Identify the blood parasite species.
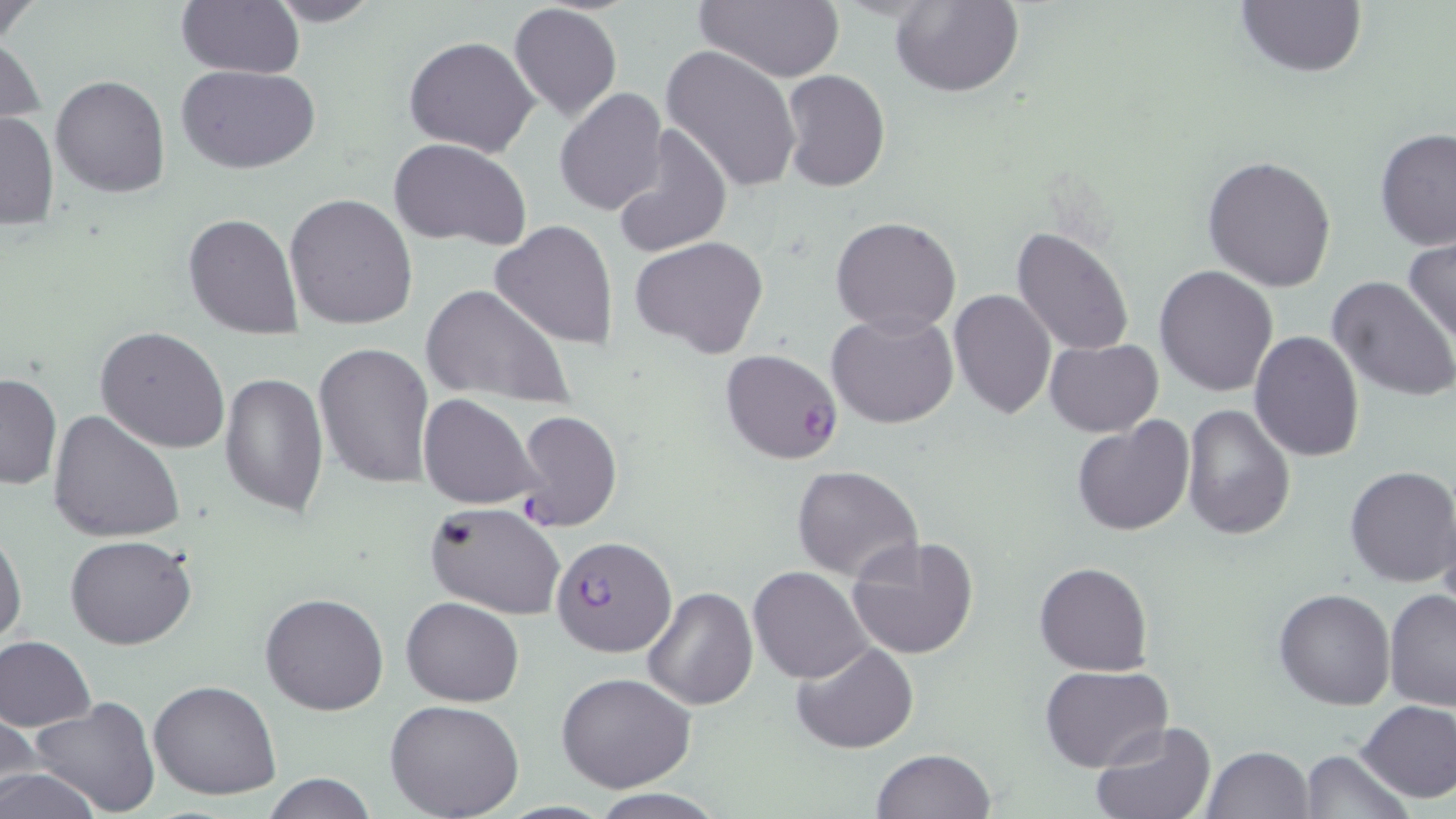
Plasmodium falciparum.

Summary:
  - Coordinate format: approximate bounding boxes as (x1, y1, x2, y2) in pixels
  - Plasmodium falciparum-infected red blood cell locations: (720, 350, 842, 464), (550, 535, 678, 657)
  - Uninfected red blood cell locations: (0, 0, 46, 49), (174, 0, 304, 78), (261, 0, 383, 26), (694, 0, 844, 81), (892, 0, 1023, 97), (1234, 1, 1367, 79), (507, 3, 623, 122), (1, 31, 47, 137), (404, 36, 540, 158), (659, 45, 801, 194), (176, 64, 322, 172), (781, 69, 890, 192), (50, 75, 170, 198), (555, 89, 670, 215), (0, 110, 59, 230), (611, 126, 733, 258), (1375, 129, 1456, 250), (387, 137, 531, 249), (1202, 154, 1337, 292), (284, 192, 419, 330), (183, 213, 303, 337), (831, 216, 962, 335), (489, 220, 620, 351), (1012, 226, 1136, 357), (1403, 234, 1456, 349), (631, 235, 770, 359), (1153, 264, 1278, 397), (1327, 275, 1456, 404), (421, 283, 572, 406), (948, 289, 1057, 419), (828, 310, 958, 429), (96, 326, 230, 454), (1248, 331, 1364, 463), (1044, 338, 1164, 435), (313, 341, 435, 488), (219, 372, 330, 517), (1, 373, 62, 491), (419, 393, 541, 510), (1181, 402, 1295, 540), (47, 408, 186, 543), (514, 408, 623, 532), (1072, 415, 1194, 537), (792, 464, 923, 584), (1343, 465, 1455, 587), (1436, 498, 1456, 618), (425, 502, 568, 620), (0, 522, 26, 647), (65, 534, 197, 650), (846, 534, 981, 660), (1034, 562, 1152, 676), (748, 565, 873, 683), (642, 587, 757, 710), (1273, 588, 1396, 710), (1383, 588, 1456, 710), (260, 592, 389, 716), (402, 597, 525, 706), (0, 635, 96, 731), (793, 641, 916, 754), (1040, 664, 1172, 771), (556, 673, 698, 791), (148, 680, 281, 802), (385, 698, 525, 819), (30, 699, 162, 818), (1357, 699, 1456, 802), (1, 705, 42, 806), (1090, 721, 1216, 819), (1201, 745, 1313, 819), (870, 748, 997, 819), (1298, 749, 1412, 819), (0, 765, 104, 819), (261, 774, 381, 818)
  - Magnification: 1000x
  - Field of view: one of a larger specimen
  - Stain: May-Grünwald-Giemsa
  - Image size: 1456×819 pixels
  - Modality: light microscopy
  - Preparation: thin blood film